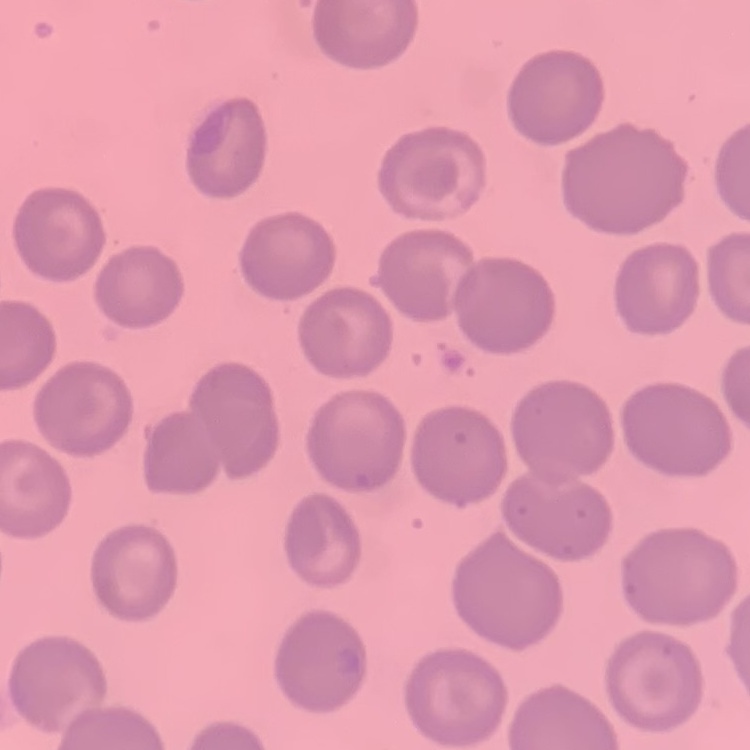
{
  "red_blood_cell_morphology": "no rouleaux formation",
  "preparation": "thin peripheral smear",
  "image_type": "one tile cut from a larger photomicrograph",
  "stain": "Field's or Giemsa"
}